Identify the parasite.
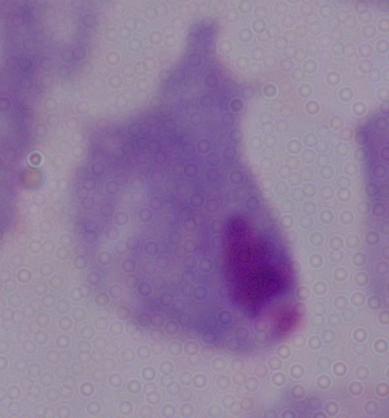

This is a trichomonad.

Summary:
  - Modality: micrograph
  - Magnification: 1000x